Locate every Plasmodium malariae-infected red blood cell.
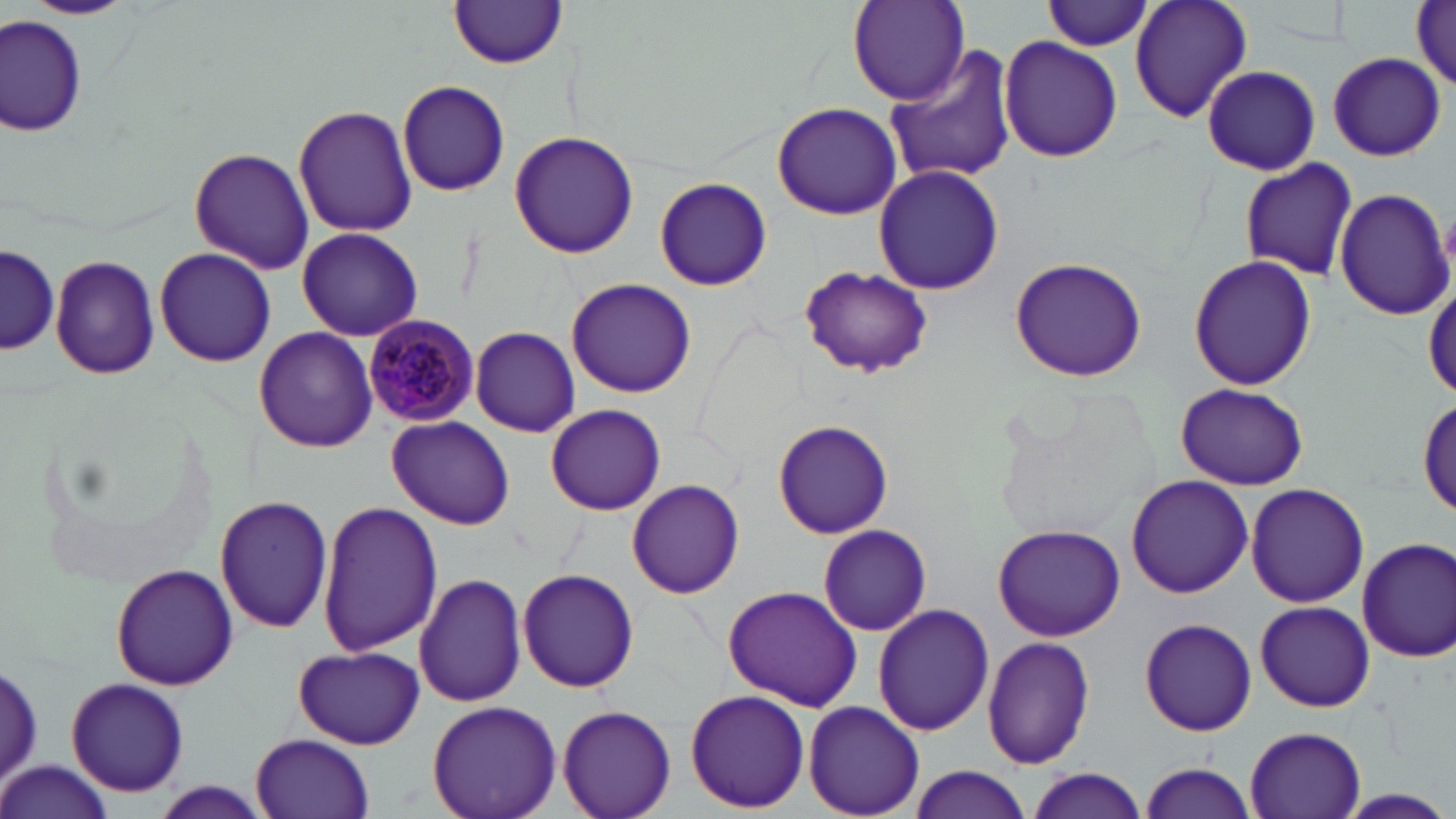
Approximate bounding boxes as (x1,y1)-(x2,y2) corner pairs in pixels.
Plasmodium malariae-infected red blood cells: (363,316)-(482,427).

slide-level diagnosis = Plasmodium malariae
magnification = 1000x
preparation = thin blood smear
stain = May-Grünwald-Giemsa
uninfected red blood cell locations = approximate bounding boxes as (x1,y1)-(x2,y2) corner pairs in pixels: (22,0)-(139,20), (846,0)-(970,107), (1130,0)-(1253,124), (1412,0)-(1456,91), (1045,1)-(1157,52), (448,2)-(568,70), (0,14)-(89,136), (999,35)-(1125,162), (883,47)-(1020,187), (1328,52)-(1445,162), (1202,66)-(1320,174), (397,80)-(511,197), (771,102)-(902,221), (293,103)-(415,238), (509,130)-(638,260), (189,147)-(314,275), (1238,157)-(1358,282), (873,164)-(1003,295), (655,176)-(773,291), (1333,187)-(1453,321), (296,227)-(423,341), (1,243)-(58,358), (154,245)-(277,368), (49,254)-(159,380), (1188,254)-(1318,393), (1010,256)-(1148,382), (800,265)-(934,377), (566,278)-(696,398), (254,326)-(378,451), (470,326)-(581,437), (1176,382)-(1308,490), (1418,396)-(1456,519), (546,403)-(665,516), (387,416)-(514,529), (772,421)-(895,540), (1126,474)-(1252,598), (627,479)-(744,599), (1244,483)-(1369,608), (214,494)-(335,634), (316,502)-(442,657), (993,523)-(1125,642), (818,524)-(931,637), (1356,537)-(1456,663), (110,566)-(237,691), (518,566)-(640,693), (414,572)-(527,707), (722,586)-(861,712), (1255,600)-(1374,712), (873,604)-(995,736), (1139,616)-(1257,736), (983,636)-(1094,768), (294,645)-(425,748), (2,659)-(44,794), (66,681)-(189,795), (685,688)-(810,813), (427,700)-(561,819), (803,701)-(927,818), (558,704)-(675,819), (1243,724)-(1367,818), (252,733)-(374,818), (2,762)-(115,819), (1140,762)-(1256,818), (905,765)-(1033,819), (1025,769)-(1149,818), (1337,788)-(1454,818)
modality = light microscopy
field of view = single
image size = 1456×819 pixels